Name the blood parasite species.
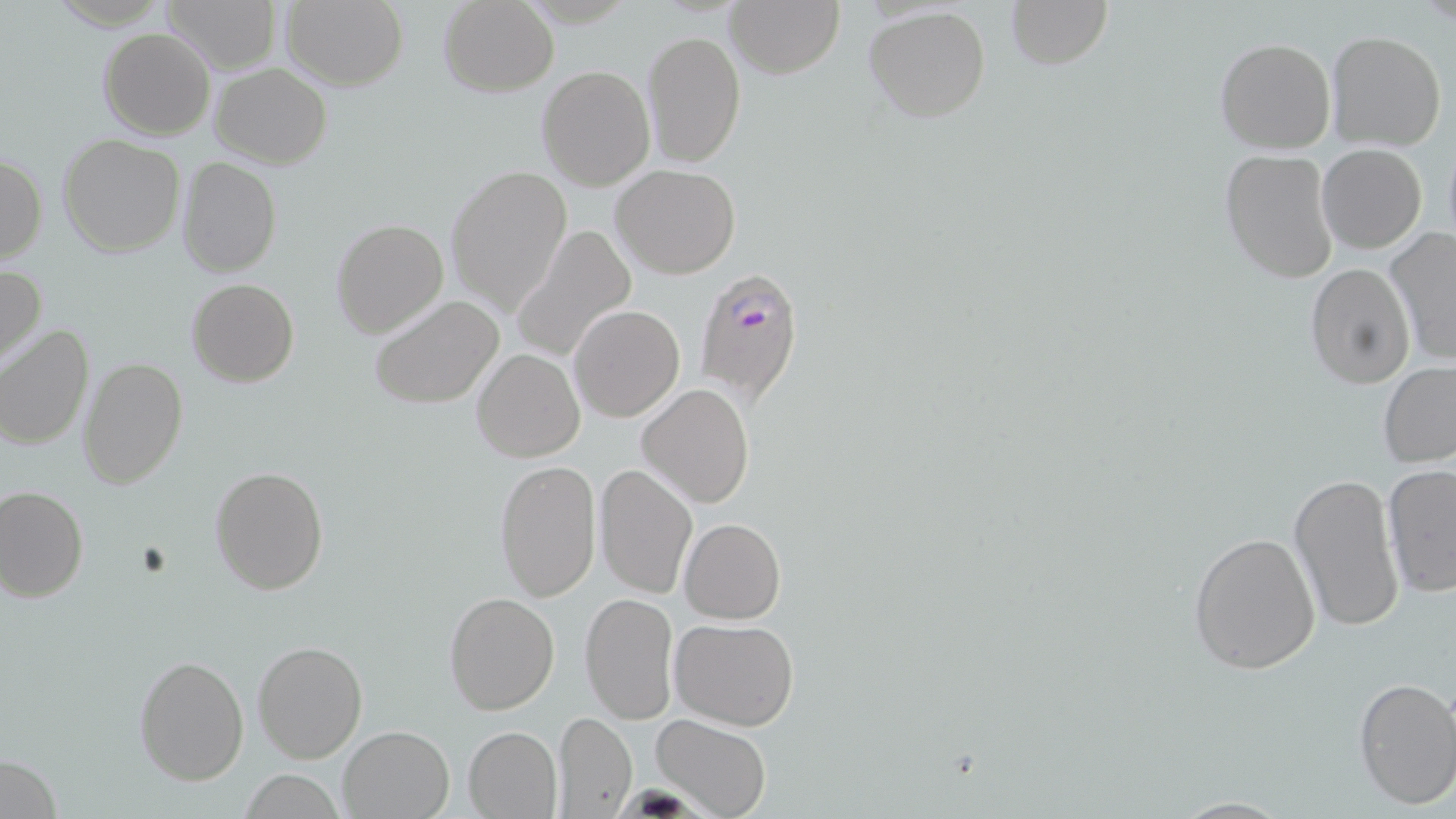

Plasmodium falciparum.

Summary:
  - Coordinate format: approximate bounding boxes as named x1/y1/x2/y2 corners in pixels
  - Uninfected red blood cell locations: (x1=163, y1=0, x2=282, y2=74), (x1=280, y1=0, x2=408, y2=90), (x1=725, y1=0, x2=844, y2=77), (x1=1006, y1=0, x2=1112, y2=69), (x1=438, y1=1, x2=559, y2=96), (x1=864, y1=6, x2=992, y2=124), (x1=98, y1=28, x2=216, y2=141), (x1=642, y1=30, x2=746, y2=169), (x1=1325, y1=30, x2=1448, y2=152), (x1=1214, y1=37, x2=1336, y2=155), (x1=537, y1=63, x2=654, y2=190), (x1=209, y1=64, x2=332, y2=168), (x1=58, y1=134, x2=186, y2=258), (x1=1316, y1=144, x2=1426, y2=253), (x1=1221, y1=150, x2=1341, y2=286), (x1=0, y1=153, x2=47, y2=265), (x1=178, y1=157, x2=282, y2=277), (x1=444, y1=164, x2=575, y2=317), (x1=612, y1=165, x2=740, y2=279), (x1=331, y1=217, x2=448, y2=338), (x1=511, y1=226, x2=637, y2=363), (x1=1384, y1=227, x2=1456, y2=367), (x1=1304, y1=263, x2=1414, y2=390), (x1=0, y1=264, x2=46, y2=371), (x1=186, y1=279, x2=299, y2=388), (x1=368, y1=292, x2=504, y2=409), (x1=571, y1=305, x2=684, y2=422), (x1=0, y1=325, x2=93, y2=449), (x1=471, y1=348, x2=585, y2=463), (x1=80, y1=357, x2=187, y2=488), (x1=1378, y1=362, x2=1456, y2=469), (x1=636, y1=383, x2=754, y2=508), (x1=493, y1=459, x2=602, y2=603), (x1=1382, y1=463, x2=1456, y2=598), (x1=594, y1=464, x2=698, y2=598), (x1=210, y1=465, x2=329, y2=596), (x1=1289, y1=471, x2=1405, y2=634), (x1=0, y1=486, x2=88, y2=603), (x1=680, y1=517, x2=786, y2=622), (x1=1189, y1=529, x2=1322, y2=674), (x1=443, y1=591, x2=559, y2=715), (x1=579, y1=591, x2=678, y2=725), (x1=670, y1=617, x2=801, y2=731), (x1=252, y1=640, x2=367, y2=763), (x1=134, y1=654, x2=248, y2=785), (x1=1352, y1=675, x2=1456, y2=810), (x1=554, y1=710, x2=637, y2=816), (x1=651, y1=714, x2=774, y2=819), (x1=337, y1=726, x2=454, y2=818), (x1=463, y1=726, x2=563, y2=817), (x1=0, y1=750, x2=62, y2=819), (x1=240, y1=770, x2=346, y2=816)
  - Plasmodium falciparum-infected red blood cell locations: (x1=692, y1=265, x2=809, y2=409)
  - Preparation: thin blood smear
  - Field of view: one of a larger specimen
  - Modality: optical microscopy
  - Stain: May-Grünwald-Giemsa
  - Image size: 1456×819 pixels
  - Magnification: 1000x